Locate every P. falciparum parasite and give its life-cycle stage, and locate every leukocyte and any debris.
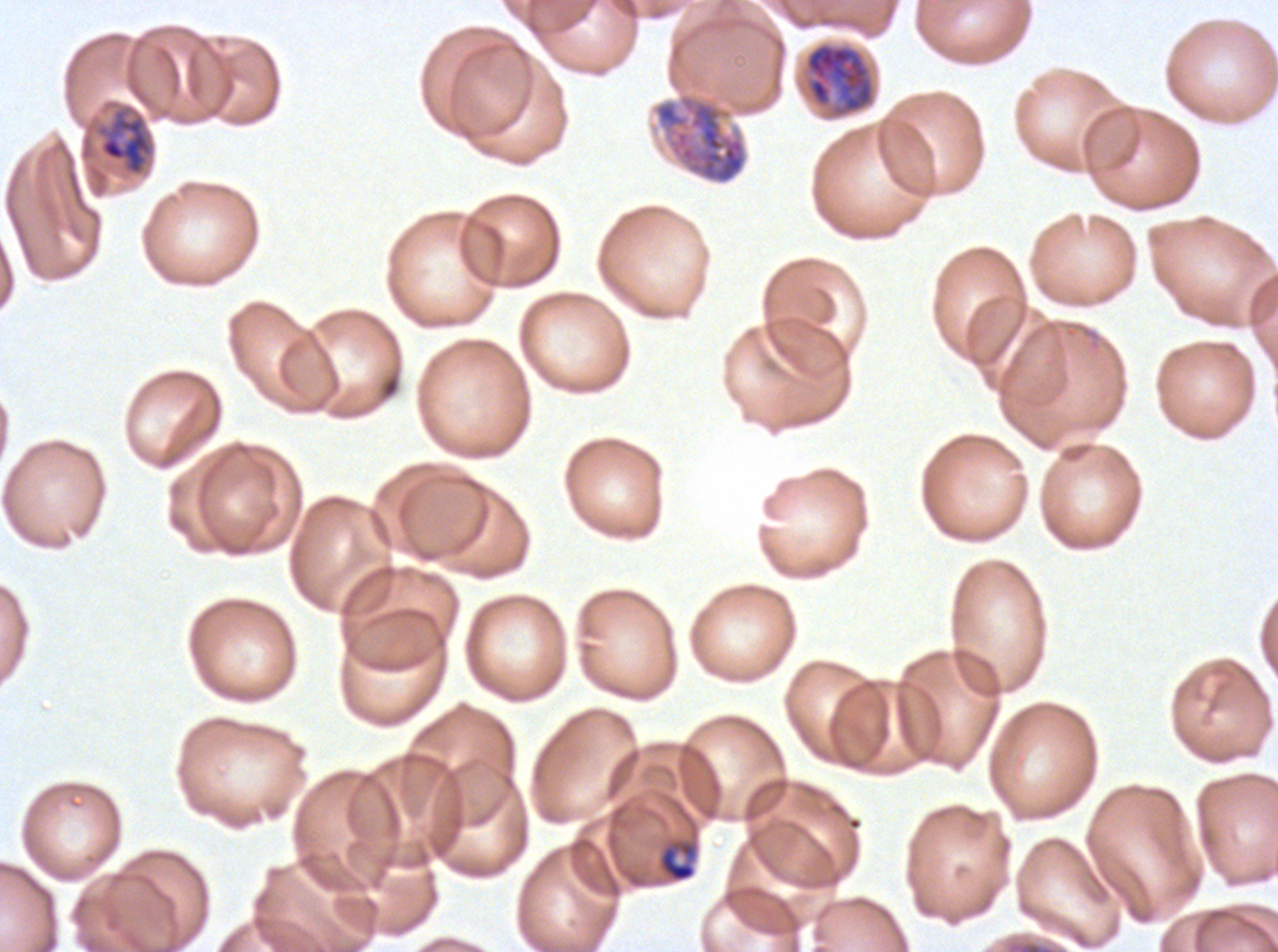

Approximate bounding rectangles given as corner coordinates in pixels from the top-left.
Late-ring/early-trophozoite forms: (x1=657, y1=837, x2=699, y2=884).
Mid trophozoites: (x1=98, y1=108, x2=154, y2=176).
Late trophozoites: (x1=651, y1=92, x2=749, y2=186).
Early schizonts: (x1=804, y1=41, x2=876, y2=119).
No rings, late schizonts, segmenters, gametocytes, leukocytes, or debris observed.

preparation = thin blood smear
stain = Giemsa
image size = 1278×952 pixels
specimen = ex-vivo P. falciparum culture from a patient in The Gambia, grown for 24 to 48 hours
life-cycle stages observed = late-ring/early-trophozoite, mid trophozoite, late trophozoite, early schizont
field of view = one sub-image of a larger composite